Classify this cell by malaria status.
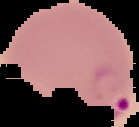

It is parasitized.

Summary:
  - Preparation: thin blood film
  - Image type: segmented cell region with the area outside set to black
  - Image size: 139×127 pixels